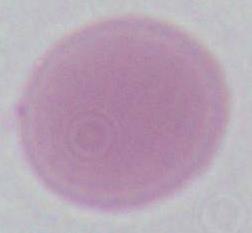
identification: red blood cell
magnification: 1000x
modality: micrograph